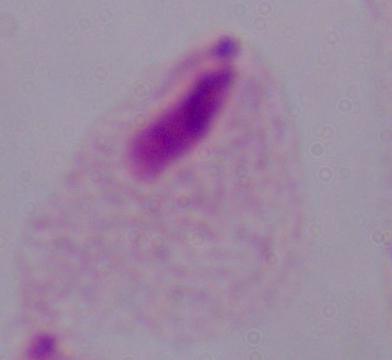
magnification: 1000x
modality: photomicrograph
identification: trichomonad